Identify the parasite.
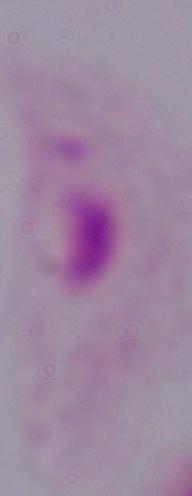

This is a trichomonad.

1000x magnification. Photomicrograph.